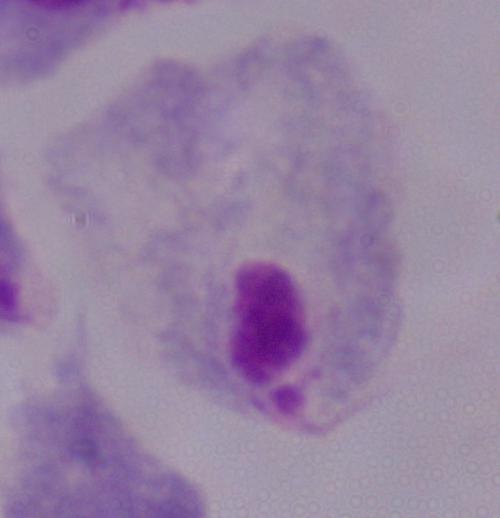

Summary:
  - Modality: micrograph
  - Magnification: 1000x
  - Identification: trichomonad